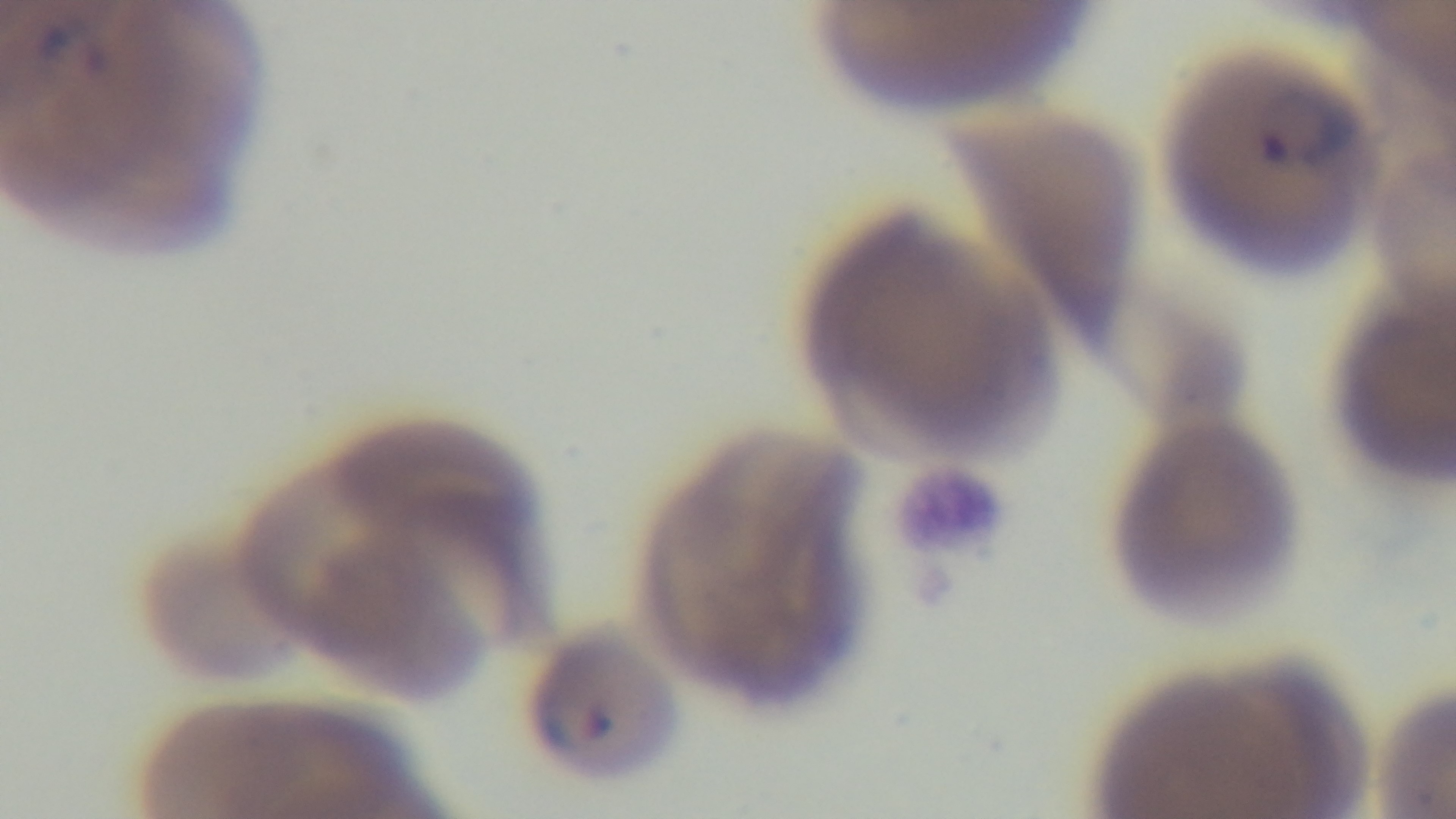

malaria status = infected
capture = mounted 4K digital camera
preparation = thin blood film
field of view = single
stain = Giemsa
modality = light microscopy
objective = 100x oil immersion